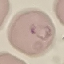

Summary:
  - Result: malaria parasites detected
  - Stain: Giemsa
  - Image type: cell patch, automatically extracted from a larger field of view and resized to 64 × 64 pixels
  - Preparation: thin blood film
  - Capture: smartphone through the microscope eyepiece